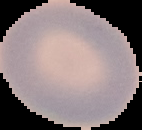 Image is 142×130 pixels. The area outside the segmented cell region is set to black. Malaria status: uninfected. From a thin blood smear.